State which parasite is depicted.
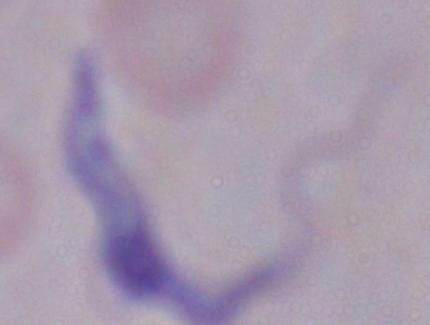
A trypanosome.

magnification = 1000x
modality = micrograph